State which parasite is depicted.
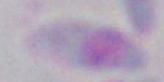

This is Toxoplasma gondii.

Summary:
  - Magnification: 1000x
  - Modality: photomicrograph